Identify the parasite.
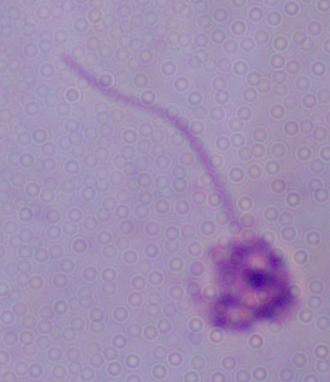

Leishmania.

{
  "modality": "photomicrograph",
  "magnification": "1000x"
}